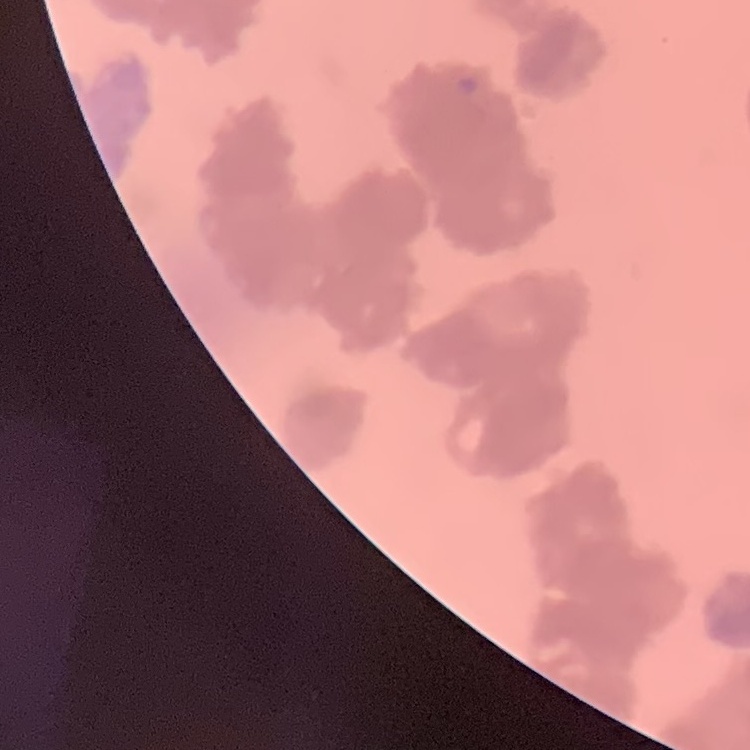

The erythrocytes show rouleaux formation. One tile cut from a larger photomicrograph. Stained with either Field's or Giemsa. Thin blood film.